Assess this cell for malaria.
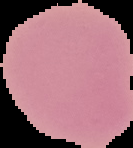

It is uninfected.

Segmented cell region on a black background. Image is 133×148 pixels. From a thin blood film.